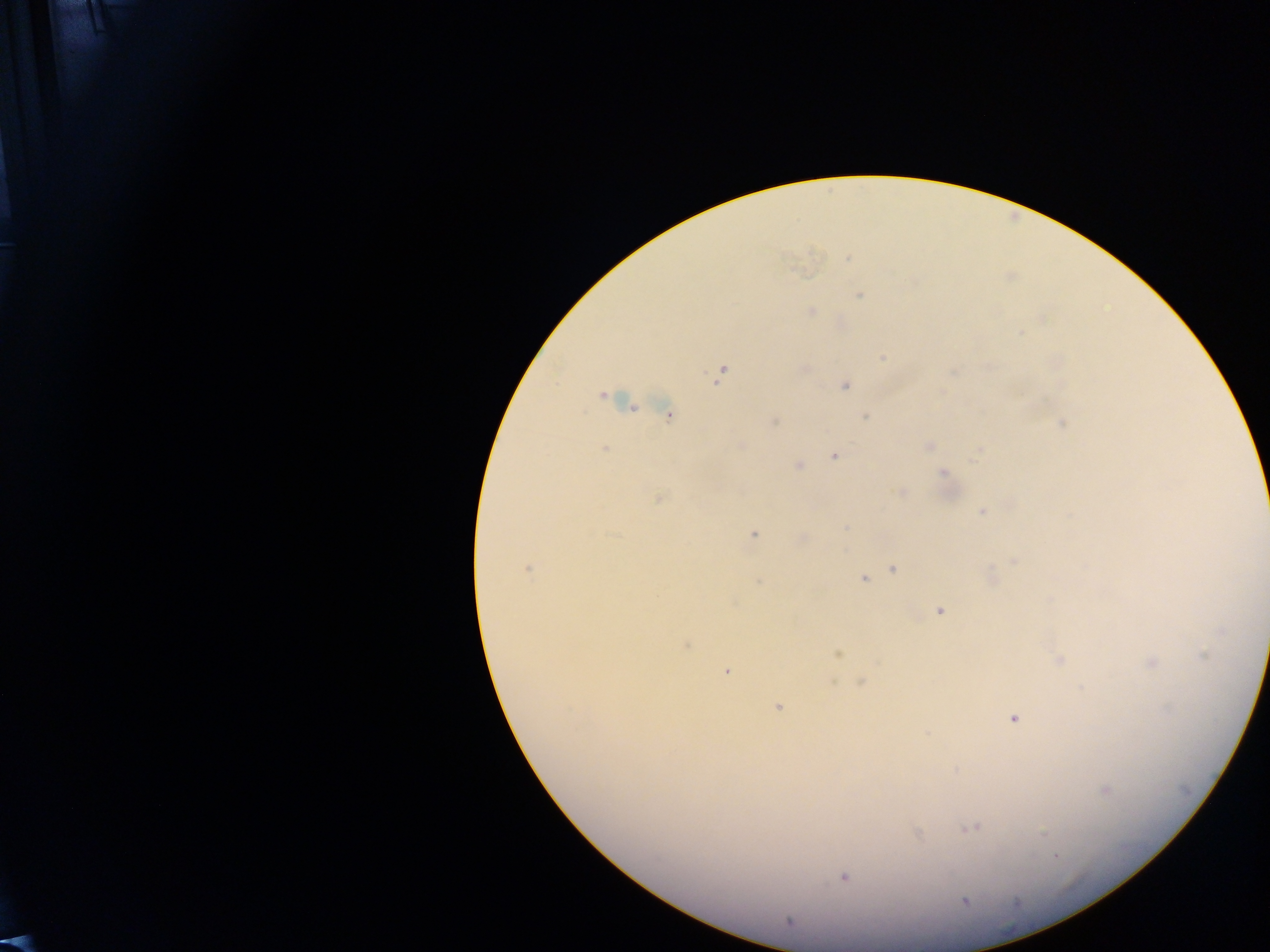
{
  "country": "Ghana",
  "field_of_view": "single",
  "malaria_parasite_locations": "approximate centers as {x, y} in pixels: {848, 259}, {859, 295}, {811, 311}, {1020, 334}, {883, 357}, {953, 372}, {720, 375}, {845, 386}, {602, 395}, {667, 415}, {865, 416}, {774, 421}, {1062, 423}, {741, 445}, {929, 446}, {605, 448}, {975, 454}, {834, 456}, {799, 466}, {943, 473}, {901, 493}, {659, 499}, {982, 512}, {753, 534}, {1013, 562}, {528, 568}, {893, 569}, {862, 579}, {758, 581}, {940, 611}, {686, 645}, {837, 654}, {1203, 656}, {1059, 660}, {1152, 663}, {726, 671}, {860, 682}, {778, 707}, {1014, 717}, {1105, 790}, {971, 828}, {1044, 833}, {917, 835}, {1056, 856}, {844, 877}, {964, 901}, {789, 921}",
  "preparation": "thick blood film",
  "capture": "mobile-phone photograph through a microscope",
  "image_size": "1270×952 pixels"
}